Locate every Plasmodium malariae-infected red blood cell.
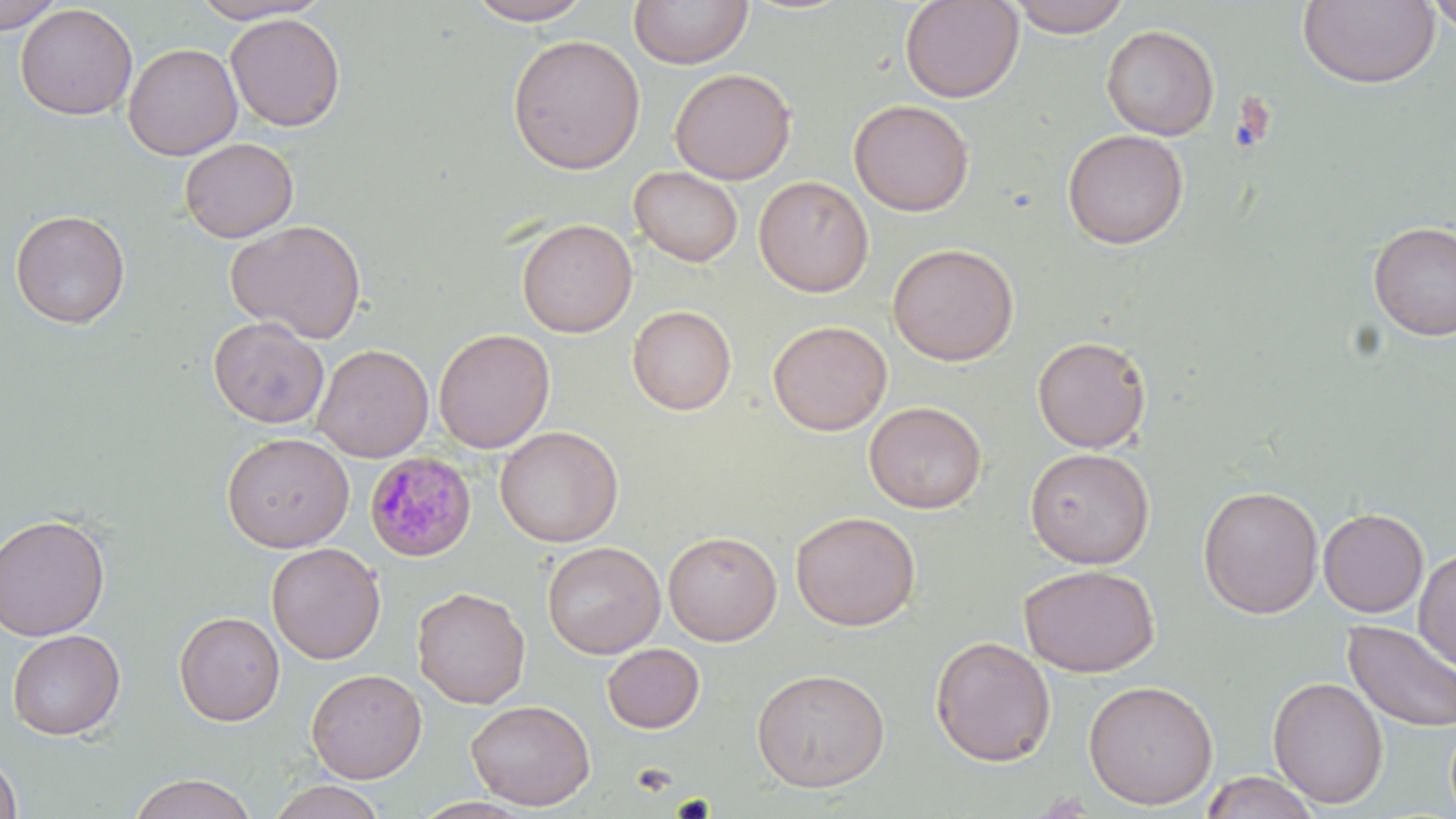
Approximate bounding boxes as (x1, y1, x2, y2) in pixels.
Plasmodium malariae-infected red blood cells: (364, 452, 477, 562).

slide_level_diagnosis: Plasmodium malariae
uninfected_red_blood_cell_locations: 'approximate bounding boxes as (x1, y1, x2, y2) in pixels: (0, 0, 64, 34), (187, 0, 331, 24), (464, 0, 596, 26), (629, 0, 753, 69), (900, 0, 1023, 103), (1008, 0, 1131, 37), (1424, 0, 1456, 41), (1297, 1, 1440, 89), (15, 3, 138, 120), (226, 13, 346, 132), (1101, 24, 1219, 140), (507, 34, 646, 175), (122, 43, 242, 160), (670, 68, 796, 184), (849, 99, 974, 216), (1062, 129, 1188, 249), (179, 137, 299, 243), (629, 166, 743, 267), (754, 175, 874, 297), (9, 208, 131, 328), (516, 218, 637, 338), (226, 219, 366, 343), (1367, 221, 1456, 341), (887, 243, 1019, 366), (627, 305, 736, 415), (208, 316, 330, 429), (768, 320, 893, 436), (432, 328, 555, 453), (1032, 335, 1152, 453), (312, 344, 434, 462), (864, 401, 987, 514), (494, 425, 624, 547), (221, 432, 355, 553), (1024, 447, 1155, 569), (1197, 485, 1324, 619), (1317, 508, 1429, 617), (790, 510, 921, 632), (0, 513, 111, 641), (663, 531, 782, 646), (541, 541, 665, 659), (266, 542, 386, 664), (1413, 548, 1456, 671), (1018, 564, 1159, 677), (412, 586, 530, 708), (173, 611, 285, 726), (1342, 620, 1456, 734), (7, 629, 126, 740), (930, 635, 1056, 766), (601, 643, 705, 733), (750, 667, 891, 793), (306, 668, 427, 784), (1267, 676, 1388, 809), (1083, 679, 1219, 810), (466, 698, 595, 811), (0, 751, 23, 818), (1201, 771, 1319, 819), (129, 772, 258, 819), (267, 780, 388, 819)'
field_of_view: one of a larger specimen
magnification: 1000x
stain: May-Grünwald-Giemsa
modality: optical microscopy
image_size: 1456×819 pixels
preparation: thin blood smear